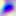

magnification: 400x
modality: micrograph
identification: Toxoplasma gondii